Assess for Plasmodium parasites.
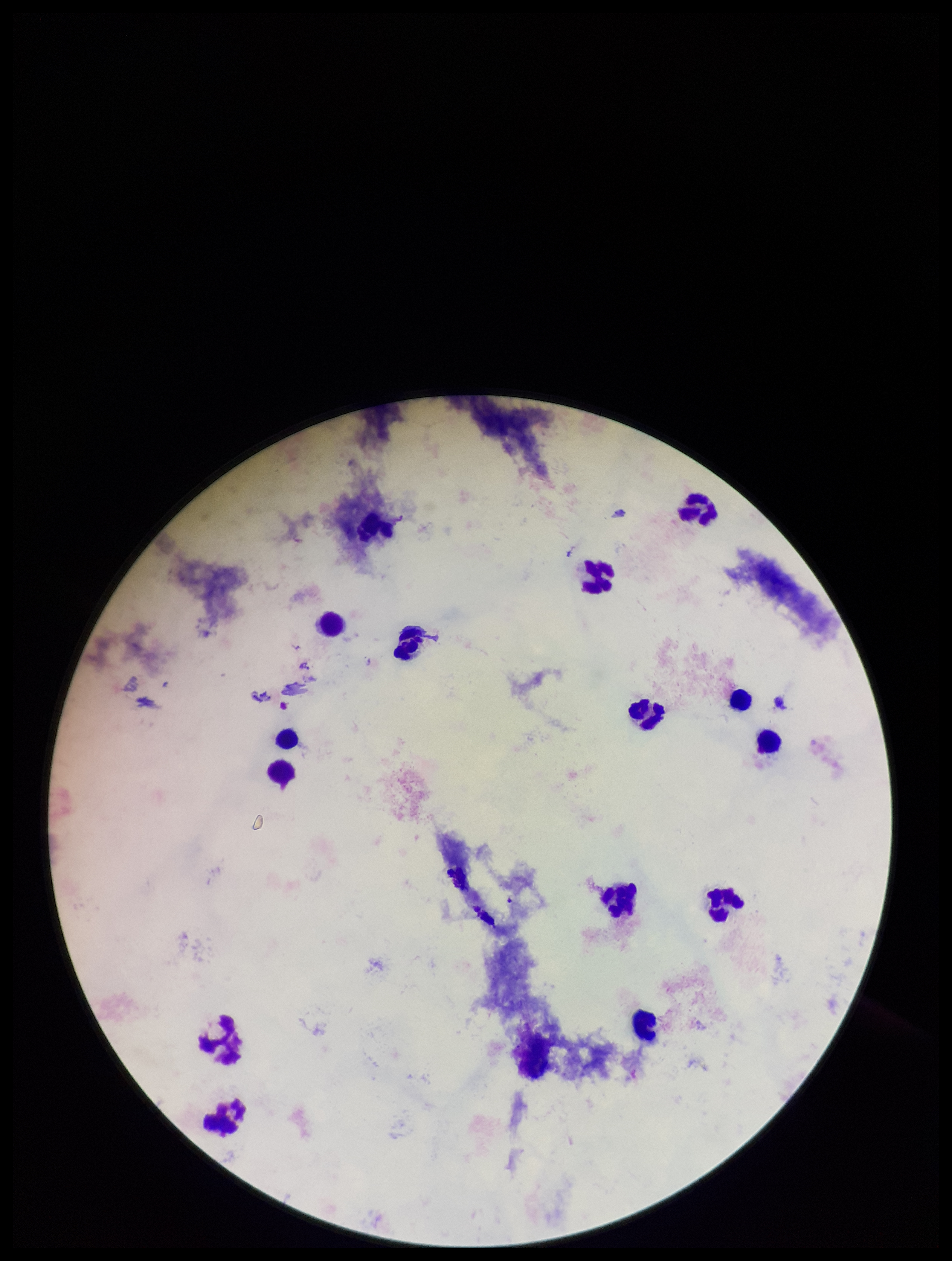

None seen.

{
  "leukocyte_count": 16,
  "preparation": "thick blood smear",
  "field_of_view": "one from this slide",
  "image_size": "952×1261 pixels",
  "stain": "Giemsa",
  "parasite_count": 0,
  "capture": "smartphone photograph through the microscope eyepiece",
  "patient_malaria_status": "negative"
}